Assess the morphology of the red blood cells.
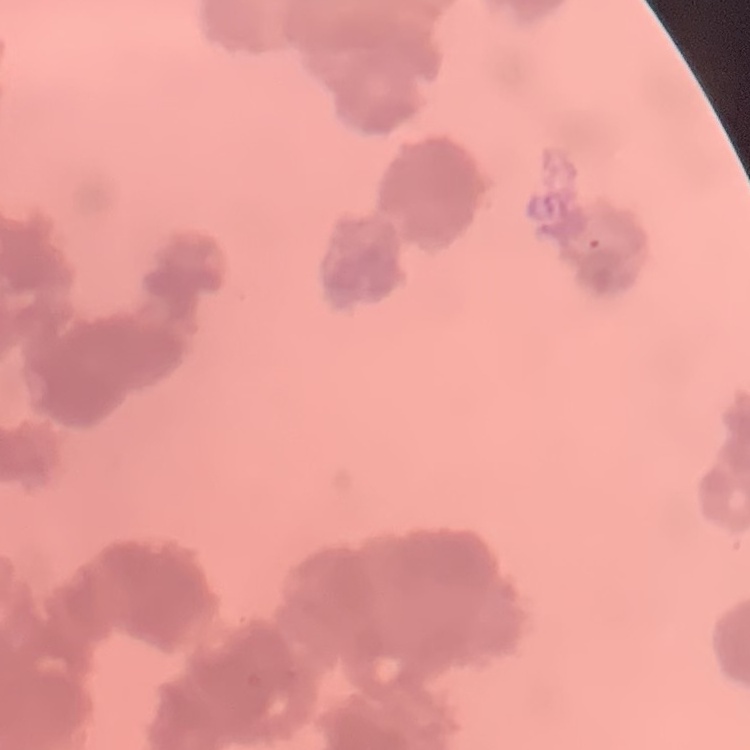

They show rouleaux formation.

{
  "image_type": "one tile cut from a larger photomicrograph",
  "stain": "Field's or Giemsa",
  "preparation": "thin blood smear"
}